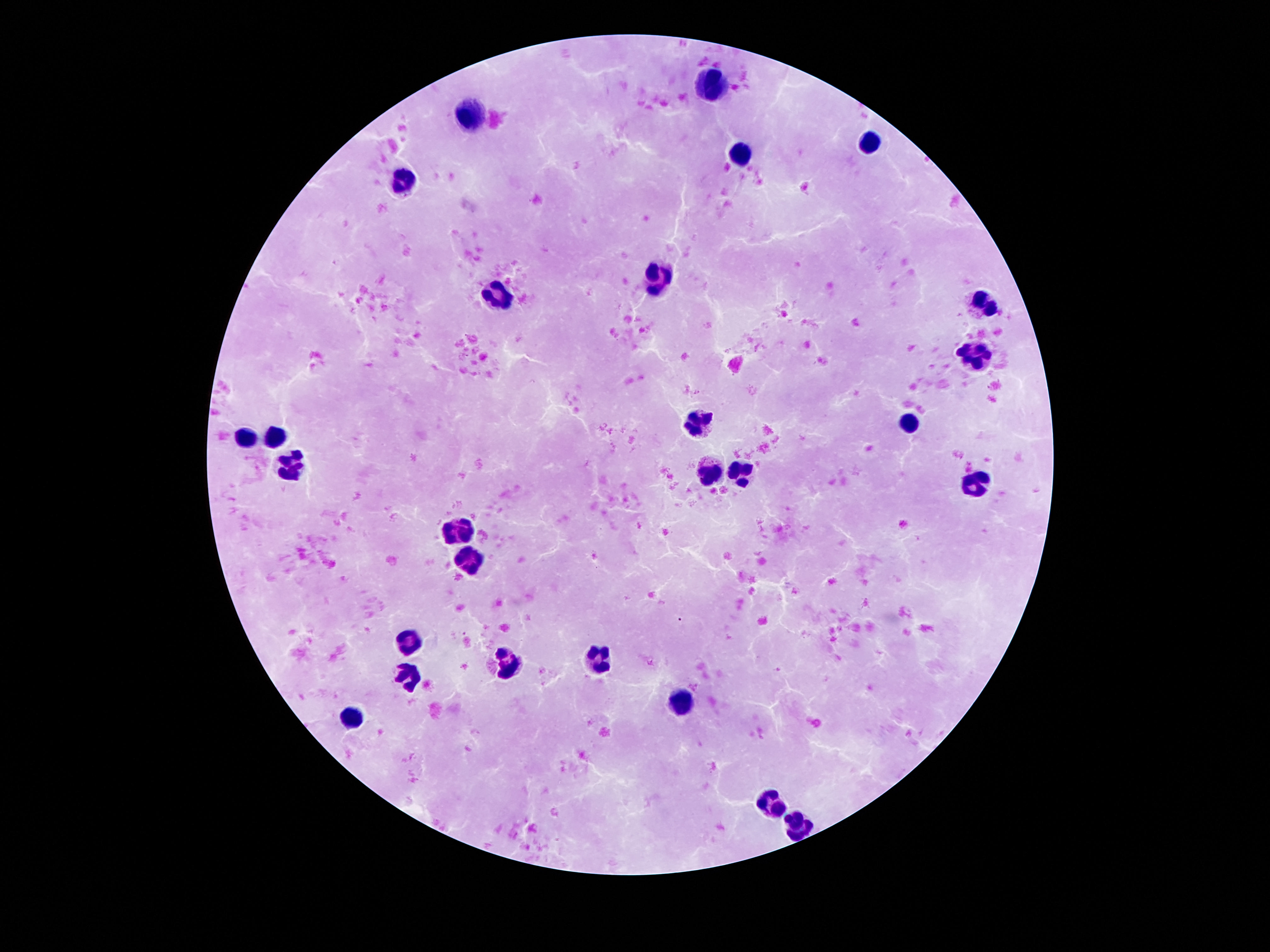

patient malaria status = negative
image size = 1270×952 pixels
capture = smartphone camera through the microscope eyepiece
stain = Giemsa
leukocyte locations = approximate centers as {x, y} in pixels: {711, 83}, {470, 113}, {870, 143}, {747, 160}, {405, 179}, {659, 276}, {496, 295}, {986, 300}, {979, 350}, {695, 422}, {909, 423}, {275, 438}, {244, 440}, {289, 463}, {713, 469}, {741, 474}, {972, 483}, {459, 531}, {468, 560}, {411, 640}, {598, 658}, {507, 664}, {409, 674}, {686, 700}, {352, 717}, {768, 803}, {799, 824}
magnification = 100x
preparation = thick blood film
field of view = one from this slide